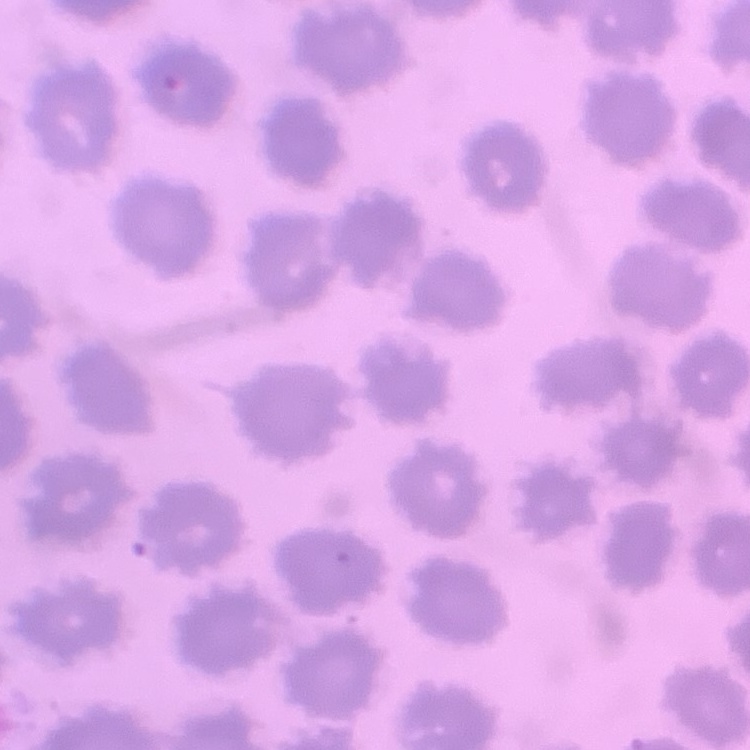

red blood cell morphology = no rouleaux formation
stain = Field's or Giemsa
image type = square crop of a larger photomicrograph
preparation = thin peripheral smear